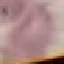
Malaria status: uninfected. Photographed with a smartphone camera at the microscope eyepiece. Giemsa-stained preparation. Thin blood smear. Cell patch, automatically extracted from a larger field of view and resized to 64 × 64 pixels.